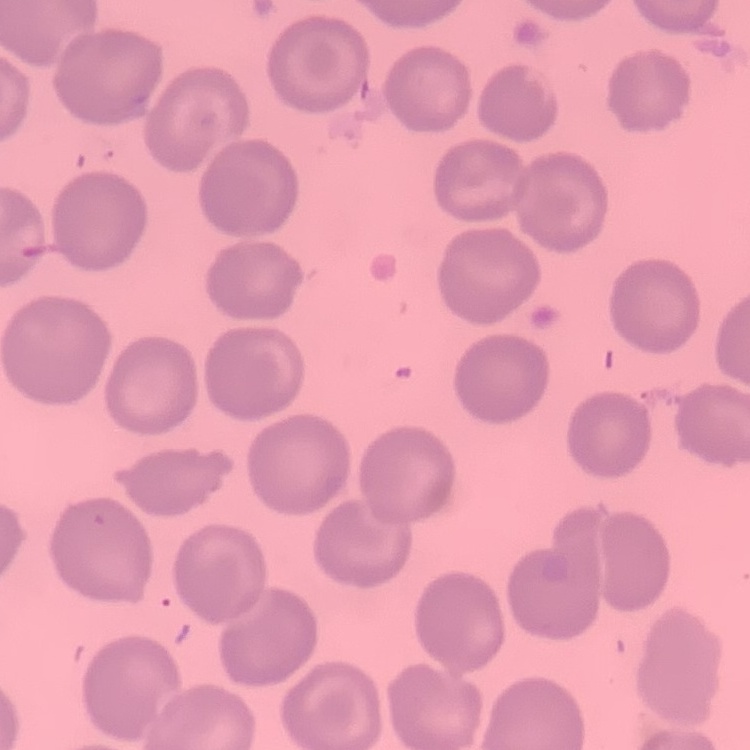
The erythrocytes exhibit no rouleaux formation. Field's or Giemsa stain. One tile cut from a larger photomicrograph. Thin blood film.